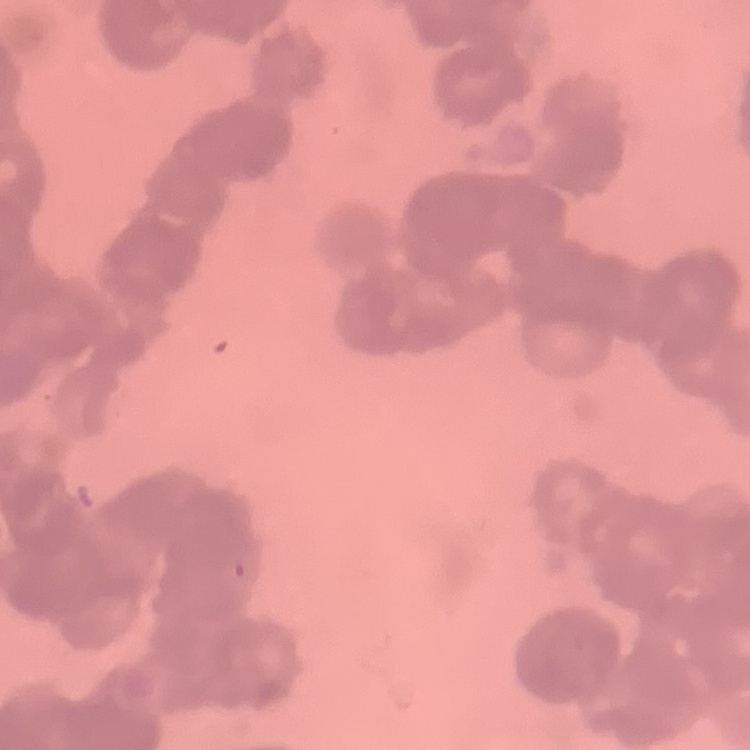 The red blood cells exhibit rouleaux formation. One tile cut from a larger photomicrograph. Field's or Giemsa stain. Thin peripheral smear.